Classify this cell by malaria status.
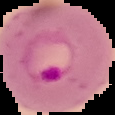

It is parasitized.

Cell region segmented out of the field of view; the surrounding area is masked to black. From a thin blood film. Image is 115×115 pixels.